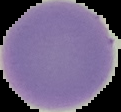
{
  "preparation": "thin blood smear",
  "image_size": "121×112 pixels",
  "result": "no malaria parasites detected",
  "image_type": "segmented cell region with the area outside set to black"
}